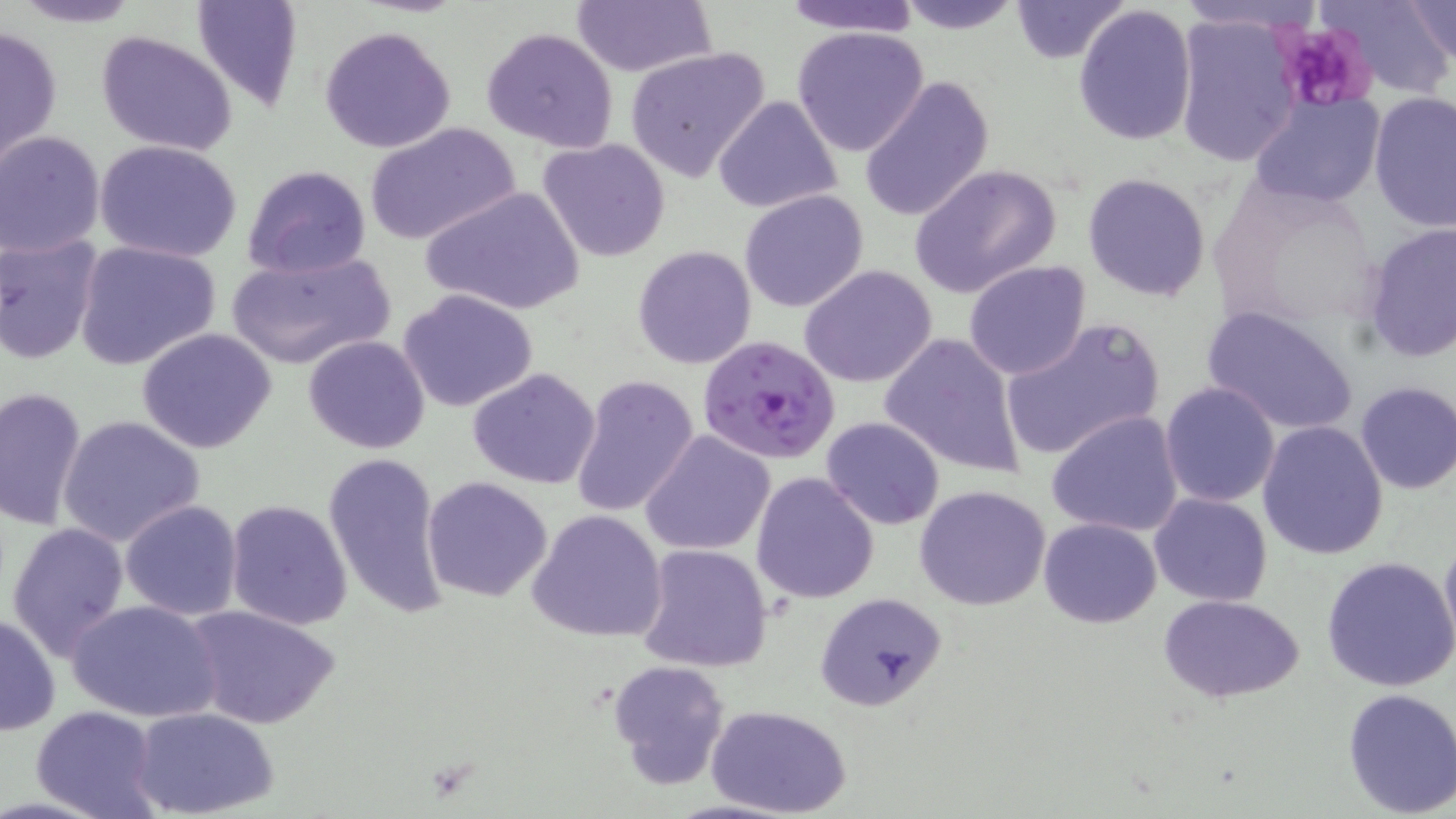
{
  "slide_level_diagnosis": "Plasmodium falciparum",
  "magnification": "1000x",
  "stain": "May-Grünwald-Giemsa",
  "platelet_locations": "approximate bounding boxes as [x1, y1, x2, y2] in pixels: [1274, 21, 1378, 114]",
  "image_size": "1456×819 pixels",
  "field_of_view": "one of a larger specimen",
  "plasmodium_falciparum_infected_red_blood_cell_locations": "approximate bounding boxes as [x1, y1, x2, y2] in pixels: [698, 334, 842, 466]",
  "modality": "optical microscopy",
  "uninfected_red_blood_cell_locations": "approximate bounding boxes as [x1, y1, x2, y2] in pixels: [6, 0, 147, 28], [190, 0, 305, 113], [777, 0, 925, 36], [897, 0, 1026, 34], [1009, 0, 1130, 63], [1318, 0, 1456, 98], [1405, 0, 1455, 67], [573, 2, 714, 76], [1072, 4, 1199, 146], [1172, 13, 1302, 167], [1, 23, 63, 167], [320, 25, 455, 153], [791, 25, 931, 158], [480, 26, 621, 153], [96, 30, 238, 158], [625, 45, 770, 181], [860, 74, 994, 221], [1368, 91, 1454, 234], [712, 94, 842, 214], [1248, 95, 1387, 208], [365, 121, 520, 245], [1, 131, 104, 257], [538, 137, 672, 262], [96, 141, 243, 262], [241, 164, 371, 279], [909, 164, 1062, 299], [1083, 171, 1213, 301], [421, 185, 584, 317], [739, 189, 870, 313], [1361, 222, 1455, 362], [0, 235, 103, 365], [73, 239, 225, 373], [632, 244, 758, 370], [226, 249, 395, 372], [963, 261, 1091, 381], [800, 265, 938, 388], [397, 289, 539, 413], [1201, 304, 1361, 438], [1000, 317, 1166, 464], [136, 328, 277, 453], [878, 332, 1028, 480], [304, 334, 429, 455], [467, 367, 602, 490], [571, 375, 700, 518], [1353, 382, 1456, 495], [1159, 383, 1281, 507], [0, 385, 88, 530], [1047, 410, 1185, 539], [56, 415, 206, 547], [821, 415, 944, 529], [1256, 420, 1388, 560], [641, 429, 776, 556], [322, 452, 449, 621], [751, 472, 880, 605], [423, 476, 553, 603], [914, 485, 1053, 612], [1149, 493, 1273, 605], [224, 499, 352, 631], [119, 500, 244, 621], [526, 509, 670, 643], [1038, 517, 1162, 627], [5, 519, 131, 662], [1439, 529, 1456, 658], [636, 542, 773, 672], [1322, 553, 1456, 692], [813, 592, 948, 711], [1158, 593, 1306, 704], [64, 598, 224, 722], [184, 603, 341, 731], [1, 611, 61, 737], [607, 659, 731, 789], [1341, 687, 1456, 817], [30, 706, 162, 818], [709, 706, 851, 818], [133, 708, 278, 817]",
  "preparation": "thin blood film"
}